Report the malaria status of this cell.
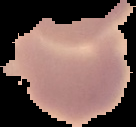
It is uninfected.

image size = 136×127 pixels
preparation = thin blood film
image type = segmented cell region on a black background